Name the blood parasite species.
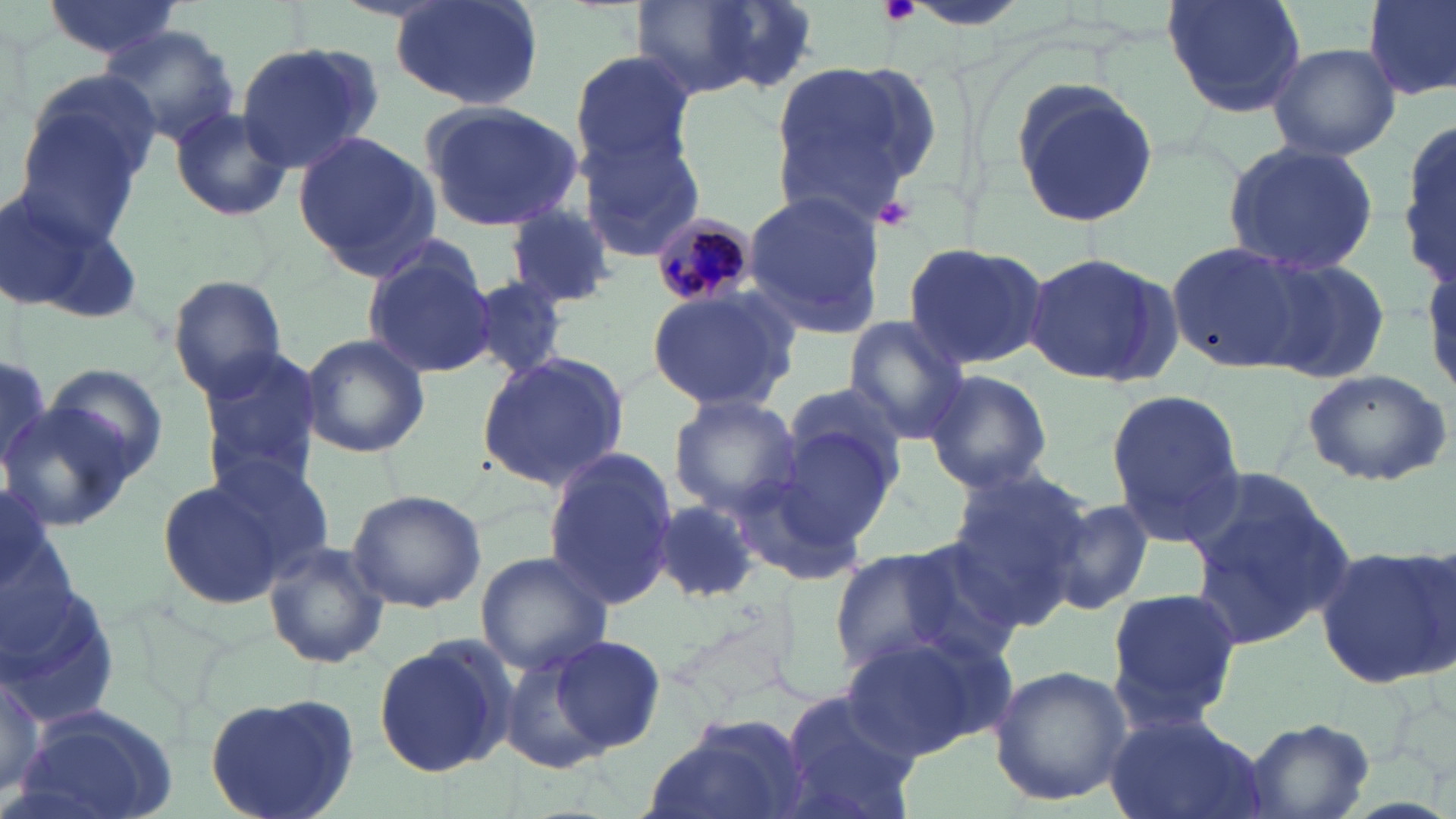

Plasmodium malariae.

Summary:
  - Coordinate format: approximate bounding boxes as named x1/y1/x2/y2 corners in pixels
  - Uninfected red blood cell locations: (x1=388, y1=0, x2=545, y2=111), (x1=1163, y1=0, x2=1307, y2=119), (x1=1362, y1=0, x2=1456, y2=100), (x1=38, y1=1, x2=186, y2=60), (x1=632, y1=2, x2=795, y2=100), (x1=100, y1=25, x2=239, y2=146), (x1=234, y1=42, x2=380, y2=174), (x1=1267, y1=42, x2=1401, y2=162), (x1=567, y1=50, x2=697, y2=172), (x1=770, y1=58, x2=940, y2=221), (x1=1008, y1=79, x2=1162, y2=229), (x1=417, y1=99, x2=587, y2=233), (x1=165, y1=106, x2=294, y2=223), (x1=14, y1=113, x2=145, y2=244), (x1=1400, y1=118, x2=1456, y2=285), (x1=292, y1=131, x2=441, y2=278), (x1=579, y1=134, x2=705, y2=263), (x1=1221, y1=141, x2=1382, y2=277), (x1=741, y1=190, x2=888, y2=332), (x1=1, y1=200, x2=138, y2=328), (x1=504, y1=204, x2=617, y2=308), (x1=1168, y1=240, x2=1319, y2=374), (x1=901, y1=241, x2=1048, y2=372), (x1=361, y1=244, x2=497, y2=381), (x1=1021, y1=249, x2=1183, y2=388), (x1=1256, y1=255, x2=1392, y2=386), (x1=167, y1=273, x2=287, y2=397), (x1=466, y1=276, x2=571, y2=382), (x1=645, y1=285, x2=799, y2=414), (x1=841, y1=318, x2=972, y2=445), (x1=299, y1=333, x2=432, y2=460), (x1=197, y1=349, x2=326, y2=495), (x1=477, y1=350, x2=631, y2=493), (x1=0, y1=357, x2=55, y2=477), (x1=39, y1=363, x2=172, y2=484), (x1=1300, y1=367, x2=1453, y2=487), (x1=922, y1=368, x2=1054, y2=495), (x1=779, y1=378, x2=912, y2=499), (x1=1104, y1=388, x2=1245, y2=545), (x1=668, y1=393, x2=805, y2=514), (x1=0, y1=402, x2=139, y2=533), (x1=744, y1=428, x2=897, y2=574), (x1=197, y1=447, x2=336, y2=580), (x1=541, y1=451, x2=678, y2=611), (x1=1181, y1=465, x2=1356, y2=653), (x1=943, y1=466, x2=1092, y2=621), (x1=156, y1=472, x2=303, y2=612), (x1=345, y1=489, x2=487, y2=613), (x1=1043, y1=497, x2=1158, y2=614), (x1=653, y1=501, x2=764, y2=605), (x1=888, y1=535, x2=1031, y2=668), (x1=262, y1=538, x2=389, y2=670), (x1=1316, y1=546, x2=1454, y2=689), (x1=827, y1=548, x2=971, y2=676), (x1=475, y1=550, x2=614, y2=676), (x1=0, y1=581, x2=126, y2=728), (x1=1106, y1=588, x2=1243, y2=727), (x1=842, y1=626, x2=1011, y2=758), (x1=373, y1=633, x2=516, y2=779), (x1=544, y1=633, x2=666, y2=755), (x1=496, y1=649, x2=619, y2=774), (x1=0, y1=655, x2=49, y2=800), (x1=987, y1=665, x2=1134, y2=804), (x1=773, y1=689, x2=924, y2=819), (x1=204, y1=694, x2=362, y2=819), (x1=11, y1=702, x2=184, y2=819), (x1=1104, y1=711, x2=1261, y2=819), (x1=645, y1=713, x2=812, y2=819), (x1=1239, y1=719, x2=1377, y2=818)
  - Platelet locations: (x1=878, y1=0, x2=920, y2=28), (x1=879, y1=198, x2=916, y2=231)
  - Plasmodium malariae-infected red blood cell locations: (x1=653, y1=213, x2=757, y2=307)
  - Magnification: 1000x
  - Stain: May-Grünwald-Giemsa
  - Preparation: thin blood smear
  - Field of view: single
  - Image size: 1456×819 pixels
  - Modality: light microscopy